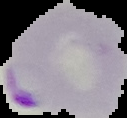

preparation = thin blood smear
image type = segmented cell region with the area outside set to black
result = Plasmodium parasites identified
image size = 127×118 pixels